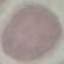 Malaria status: uninfected. Thin smear of blood. Giemsa stain. Cell patch, automatically extracted from a larger field of view and resized to 64 × 64 pixels. Photographed with a smartphone camera at the microscope eyepiece.